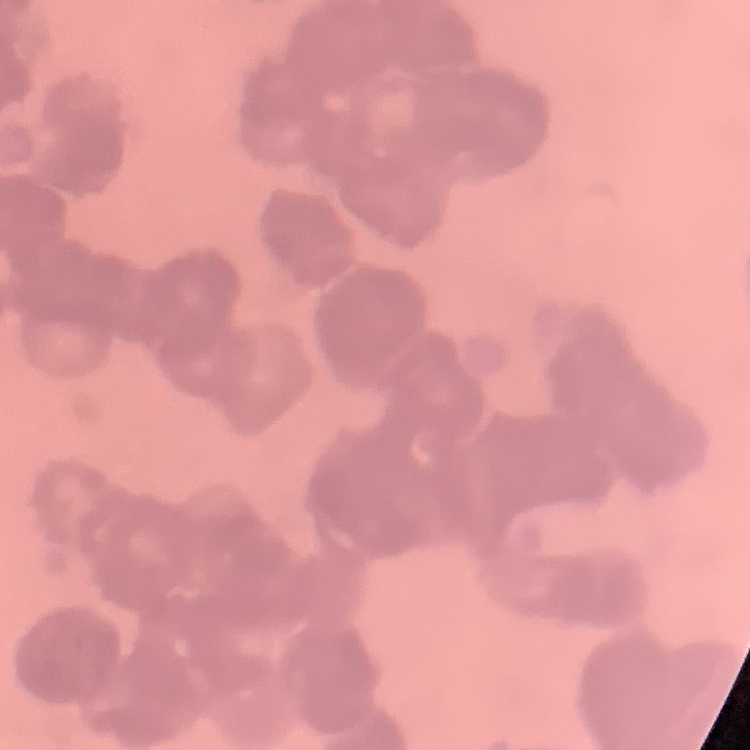
The erythrocytes show rouleaux formation. Thin peripheral smear. One tile cut from a larger photomicrograph. Field's or Giemsa stain.